Assess this cell for malaria.
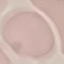
Uninfected.

capture = smartphone through the microscope eyepiece
stain = Giemsa
image type = automatically extracted cell patch, resized to 64 × 64 pixels
preparation = thin blood film